Report the malaria status of this cell.
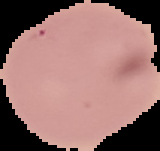

It is uninfected.

image type = segmented cell region with the area outside set to black
preparation = thin blood smear
image size = 160×151 pixels